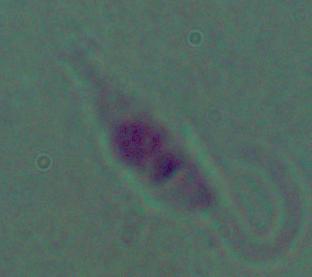

magnification = 1000x
identification = Leishmania
modality = micrograph